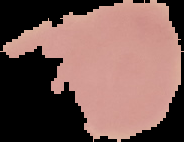

Summary:
  - Image size: 184×142 pixels
  - Malaria status: uninfected
  - Preparation: thin blood smear
  - Image type: cell region segmented out of the field of view; surrounding area masked to black